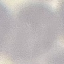

Malaria status: uninfected. Cell patch, automatically extracted from a larger field of view and resized to 64 × 64 pixels. Thin blood smear. Photographed with a smartphone camera at the microscope eyepiece. Giemsa stain.